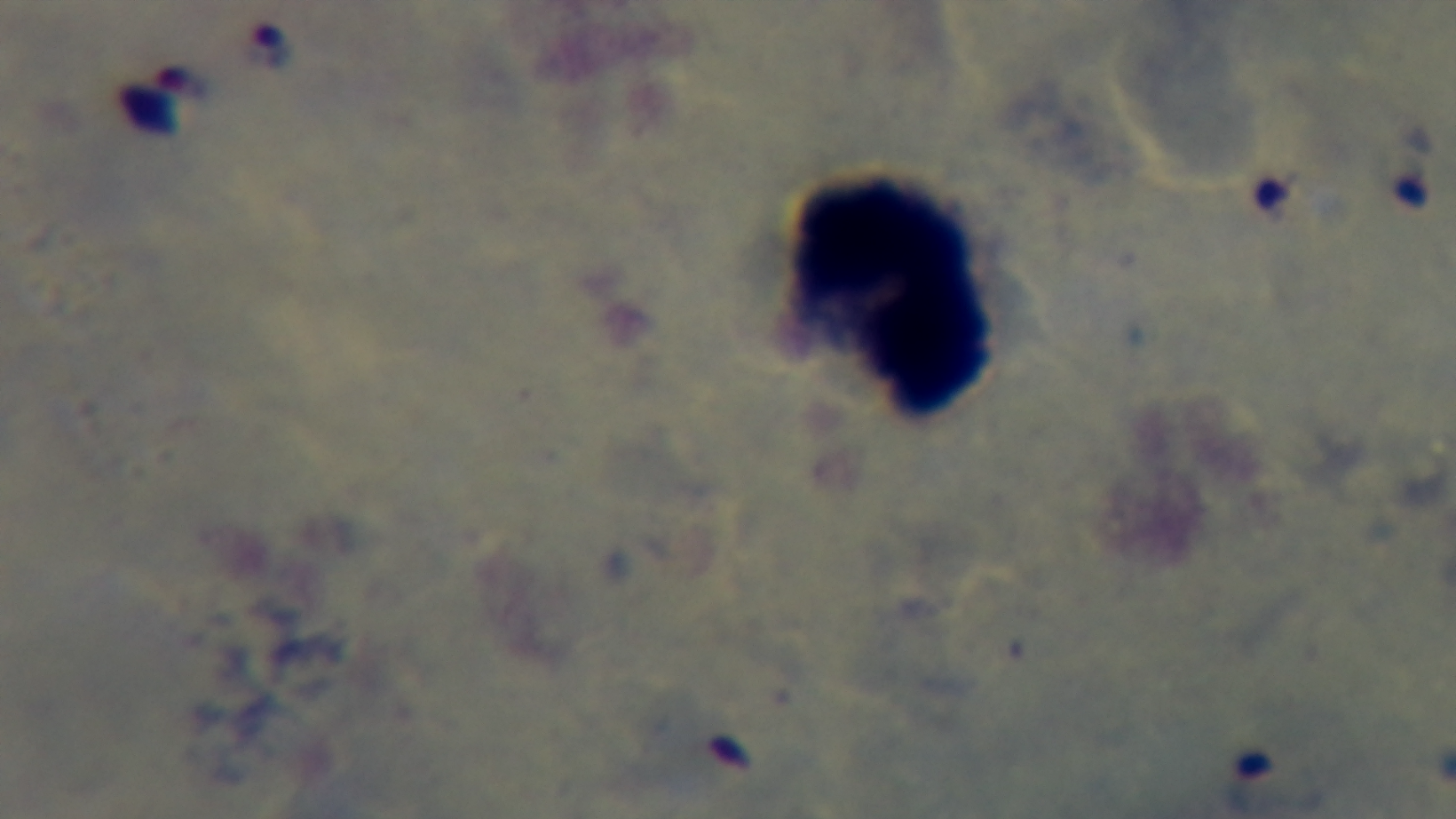
stain = Giemsa
objective = 100x oil immersion
malaria status = positive
modality = light microscopy
field of view = one from the slide
preparation = thick blood film
capture = mounted 4K digital camera